Assess this cell for malaria.
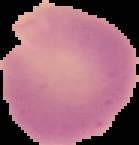
Uninfected.

Summary:
  - Preparation: thin blood film
  - Image size: 139×145 pixels
  - Image type: segmented cell region on a black background